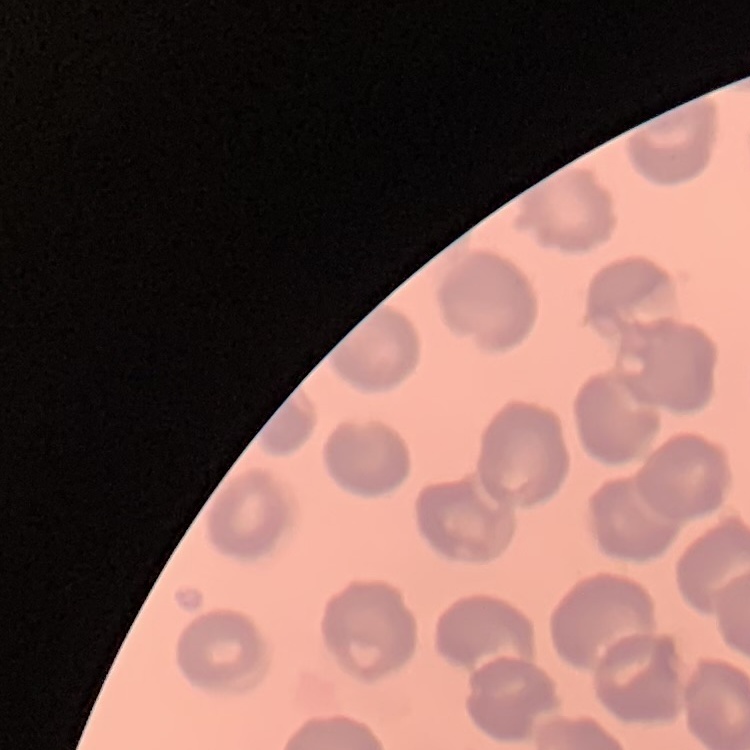

Summary:
  - Red blood cell morphology: no rouleaux formation
  - Image type: square crop of a larger photomicrograph
  - Preparation: thin blood smear
  - Stain: Field's or Giemsa